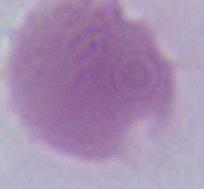 Photomicrograph. A red blood cell is shown. Captured at 1000x magnification.